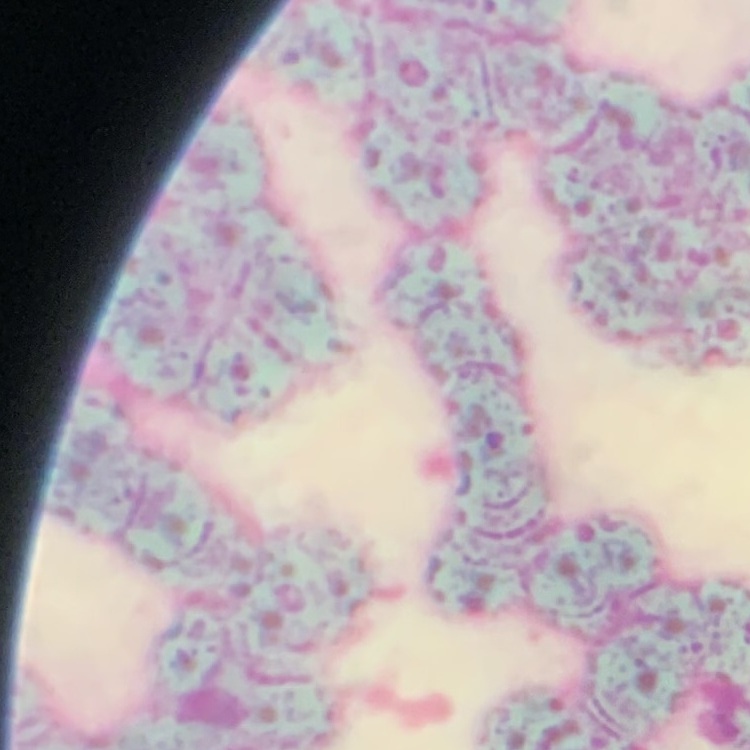
erythrocyte morphology = rouleaux formation
image type = one tile cut from a larger photomicrograph
stain = Field's or Giemsa
preparation = thin blood smear